Report the malaria status of this cell.
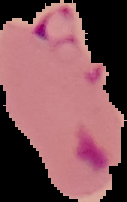

Parasitized.

Segmented cell region on a black background. From a thin blood film. Image is 127×202 pixels.